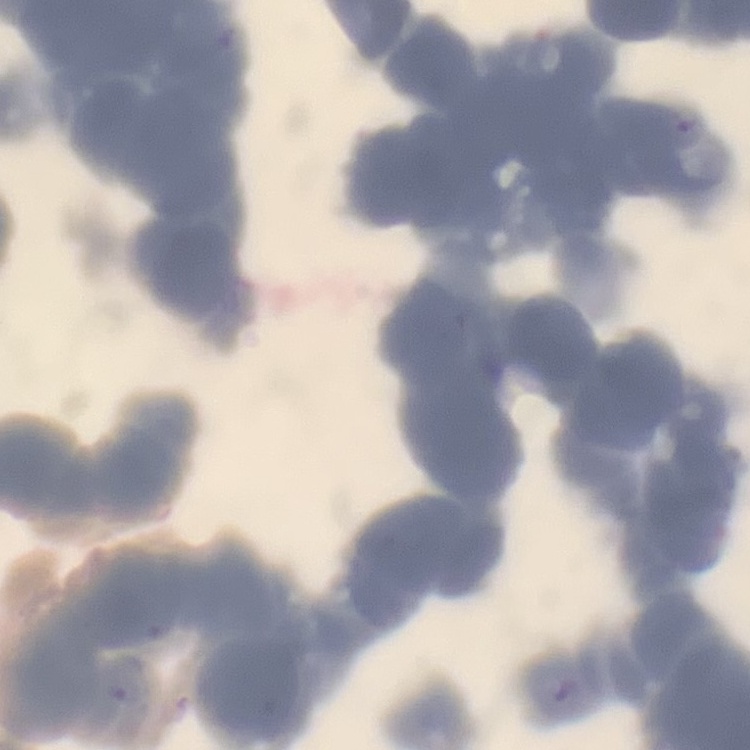
Summary:
  - Erythrocyte morphology: rouleaux formation
  - Stain: Field's or Giemsa
  - Image type: square crop of a larger photomicrograph
  - Preparation: thin blood smear